State which cell type is depicted.
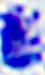
This is a leukocyte.

Captured at 400x magnification. Micrograph.